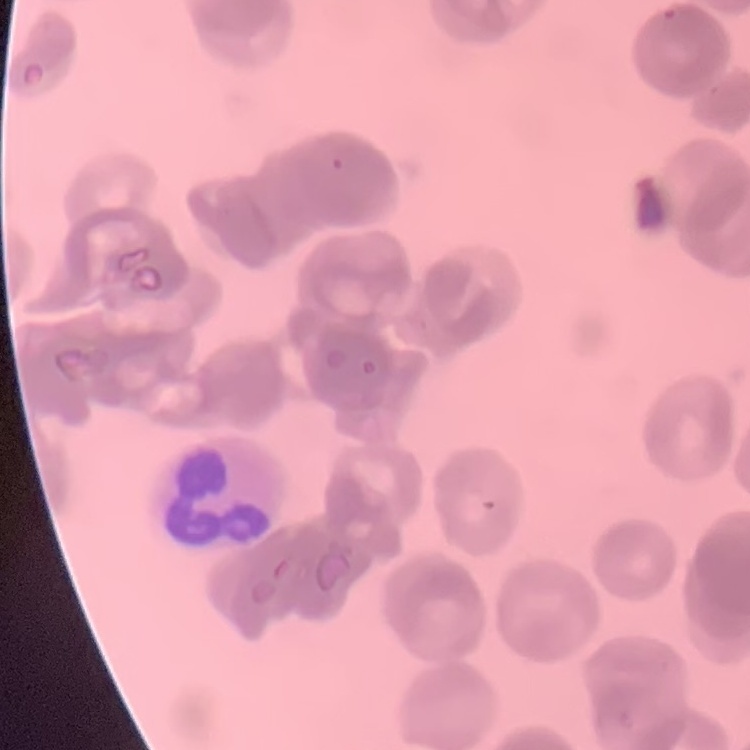

Summary:
  - Erythrocyte morphology: rouleaux formation
  - Preparation: thin blood smear
  - Stain: Field's or Giemsa
  - Image type: one tile cut from a larger photomicrograph